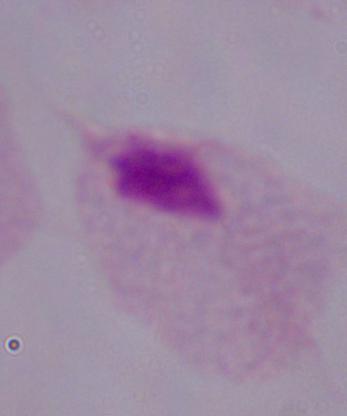
modality = photomicrograph
magnification = 1000x
identification = trichomonad